Identify the parasite.
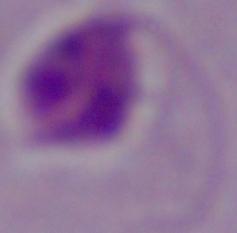
Leishmania.

Micrograph. Captured at 1000x magnification.